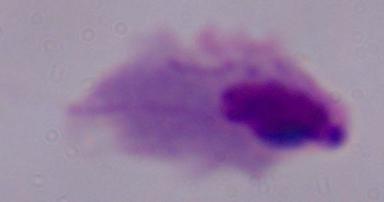

Summary:
  - Magnification: 1000x
  - Modality: photomicrograph
  - Identification: trichomonad